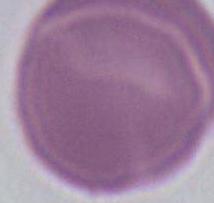
1000x magnification. Micrograph. A red blood cell is shown.